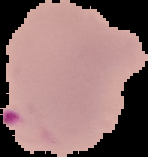

From a thin blood film. Image is 148×157 pixels. The area outside the segmented cell region is set to black. Result: malaria parasites detected.